Classify the preparation.
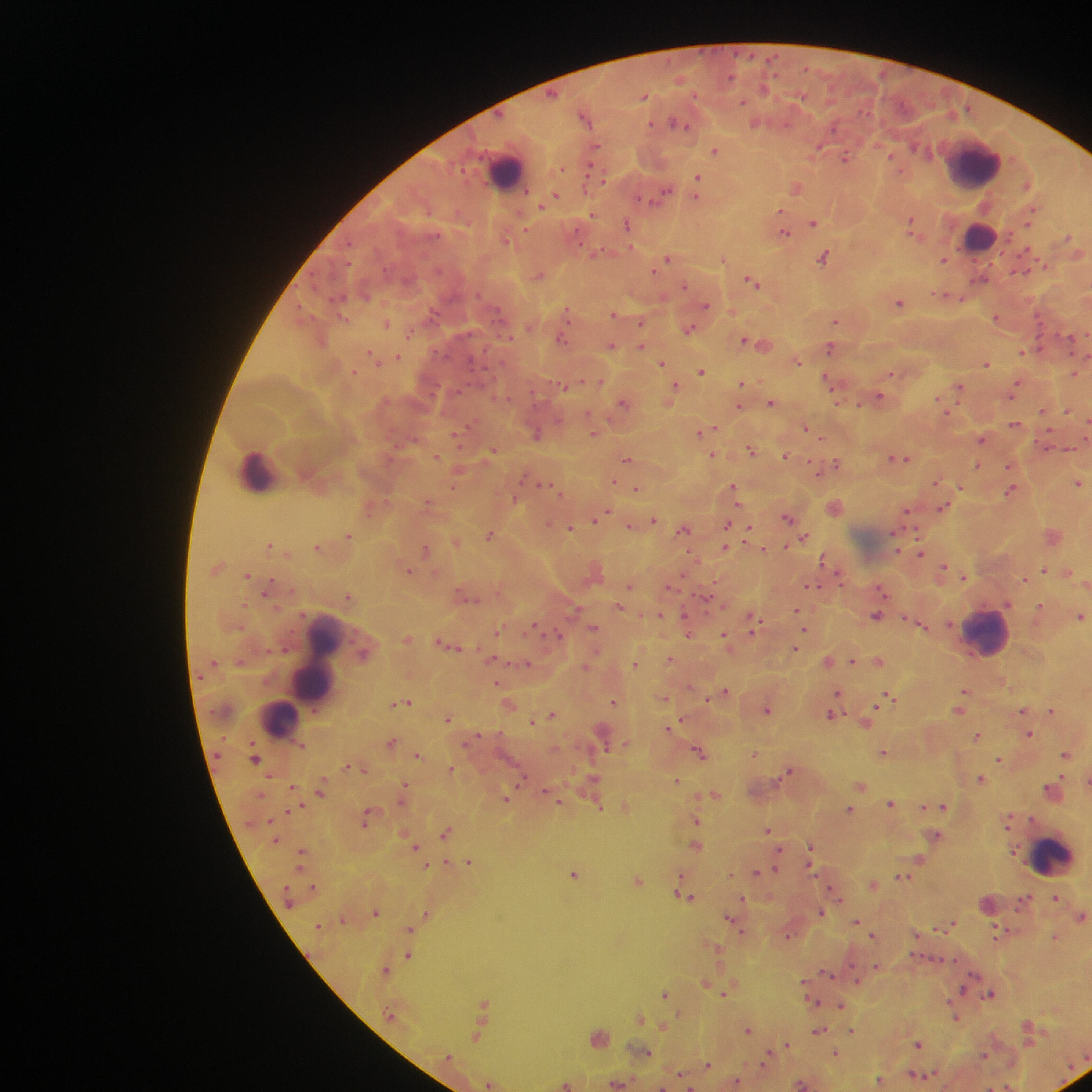

This is a thick smear.

Approximate centers as {x, y} in pixels. Leukocyte locations: {972, 164}, {506, 172}, {980, 238}, {262, 470}, {986, 634}, {321, 656}, {285, 719}, {1054, 859}. Plasmodium parasite locations: {806, 68}, {776, 76}, {644, 96}, {672, 122}, {650, 125}, {785, 125}, {687, 126}, {835, 129}, {598, 146}, {915, 146}, {820, 148}, {715, 150}, {891, 154}, {846, 157}, {590, 165}, {563, 168}, {589, 170}, {902, 171}, {699, 175}, {605, 180}, {1027, 185}, {584, 188}, {796, 188}, {668, 190}, {527, 192}, {556, 194}, {696, 196}, {639, 199}, {651, 202}, {541, 208}, {781, 210}, {592, 213}, {910, 219}, {626, 223}, {814, 223}, {526, 229}, {785, 232}, {913, 235}, {1070, 235}, {508, 240}, {583, 246}, {631, 246}, {824, 257}, {667, 258}, {945, 260}, {1046, 265}, {654, 270}, {748, 279}, {757, 285}, {685, 286}, {941, 294}, {479, 296}, {947, 296}, {339, 297}, {963, 299}, {900, 304}, {705, 306}, {568, 311}, {432, 312}, {614, 315}, {345, 317}, {569, 319}, {996, 319}, {643, 321}, {837, 321}, {386, 323}, {691, 328}, {411, 333}, {509, 337}, {562, 337}, {745, 338}, {564, 340}, {611, 345}, {642, 345}, {829, 348}, {372, 351}, {1022, 351}, {399, 356}, {662, 362}, {799, 362}, {987, 363}, {701, 372}, {353, 373}, {1075, 373}, {892, 374}, {582, 379}, {1018, 381}, {828, 383}, {741, 384}, {563, 386}, {677, 386}, {959, 387}, {879, 395}, {508, 399}, {1013, 399}, {939, 400}, {622, 402}, {772, 402}, {859, 404}, {839, 405}, {740, 406}, {947, 411}, {1068, 411}, {1041, 412}, {1016, 425}, {714, 427}, {807, 427}, {1049, 430}, {456, 433}, {594, 433}, {699, 434}, {536, 436}, {821, 440}, {982, 441}, {750, 448}, {494, 449}, {714, 454}, {438, 455}, {786, 456}, {891, 457}, {628, 459}, {898, 459}, {906, 459}, {811, 461}, {837, 463}, {978, 464}, {1008, 467}, {615, 480}, {937, 483}, {1079, 483}, {544, 484}, {960, 487}, {637, 489}, {1013, 489}, {562, 494}, {735, 496}, {428, 501}, {738, 505}, {942, 507}, {608, 511}, {906, 511}, {788, 518}, {653, 520}, {594, 522}, {549, 524}, {631, 526}, {571, 528}, {686, 528}, {915, 529}, {748, 535}, {350, 536}, {489, 536}, {804, 537}, {454, 540}, {746, 542}, {269, 545}, {786, 546}, {726, 547}, {427, 549}, {764, 549}, {921, 553}, {821, 560}, {945, 565}, {1045, 568}, {410, 570}, {1070, 573}, {684, 575}, {248, 576}, {272, 579}, {1025, 579}, {819, 585}, {630, 587}, {813, 588}, {881, 589}, {264, 593}, {883, 593}, {348, 596}, {704, 597}, {243, 605}, {1008, 605}, {1041, 605}, {796, 609}, {660, 614}, {686, 616}, {1082, 618}, {537, 626}, {594, 628}, {240, 629}, {804, 630}, {753, 631}, {497, 632}, {724, 633}, {560, 634}, {688, 635}, {442, 642}, {284, 648}, {267, 649}, {796, 649}, {596, 651}, {671, 659}, {852, 661}, {215, 662}, {528, 663}, {635, 663}, {497, 682}, {726, 690}, {838, 691}, {965, 691}, {889, 694}, {665, 698}, {706, 699}, {409, 702}, {614, 702}, {879, 702}, {401, 704}, {393, 705}, {877, 706}, {768, 711}, {1052, 711}, {830, 714}, {553, 715}, {448, 718}, {682, 718}, {533, 721}, {671, 725}, {668, 728}, {481, 733}, {1030, 733}, {978, 735}, {392, 741}, {467, 743}, {625, 743}, {606, 748}, {699, 751}, {1066, 754}, {418, 755}, {755, 755}, {216, 757}, {1000, 759}, {256, 761}, {454, 769}, {789, 770}, {785, 774}, {1061, 776}, {592, 777}, {523, 778}, {981, 778}, {676, 782}, {406, 784}, {292, 786}, {699, 795}, {507, 799}, {401, 802}, {560, 802}, {891, 802}, {302, 805}, {923, 808}, {945, 808}, {288, 810}, {851, 810}, {369, 812}, {1011, 817}, {1031, 818}, {697, 821}, {364, 823}, {1007, 826}, {768, 829}, {447, 831}, {936, 836}, {694, 845}, {811, 845}, {416, 848}, {781, 850}, {303, 851}, {919, 859}, {447, 860}, {469, 863}, {427, 865}, {809, 865}, {301, 868}, {776, 869}, {757, 871}, {574, 874}, {682, 876}, {638, 880}, {313, 885}, {831, 887}, {742, 897}, {1054, 897}, {691, 898}, {840, 899}, {376, 911}, {426, 911}, {821, 912}, {729, 917}, {344, 920}, {855, 921}, {953, 921}, {409, 930}, {872, 935}, {918, 936}, {1055, 936}, {715, 946}, {406, 956}, {935, 958}, {954, 959}, {877, 965}, {386, 968}, {831, 975}, {804, 980}, {857, 980}, {706, 982}, {963, 989}, {724, 991}, {665, 992}, {989, 994}, {817, 1000}, {949, 1000}, {484, 1002}, {841, 1005}, {679, 1013}, {639, 1016}, {958, 1018}, {1028, 1023}, {662, 1028}, {747, 1030}, {820, 1030}, {852, 1030}, {476, 1035}, {1030, 1043}, {919, 1044}, {787, 1045}, {767, 1049}, {836, 1054}, {986, 1054}, {707, 1064}, {761, 1064}, {914, 1074}, {738, 1083}, {802, 1083}, {488, 1084}, {693, 1086}. Collected in Ghana. Single field of view. Image is 1092×1092 pixels. Photographed through a microscope with a mobile-phone camera.